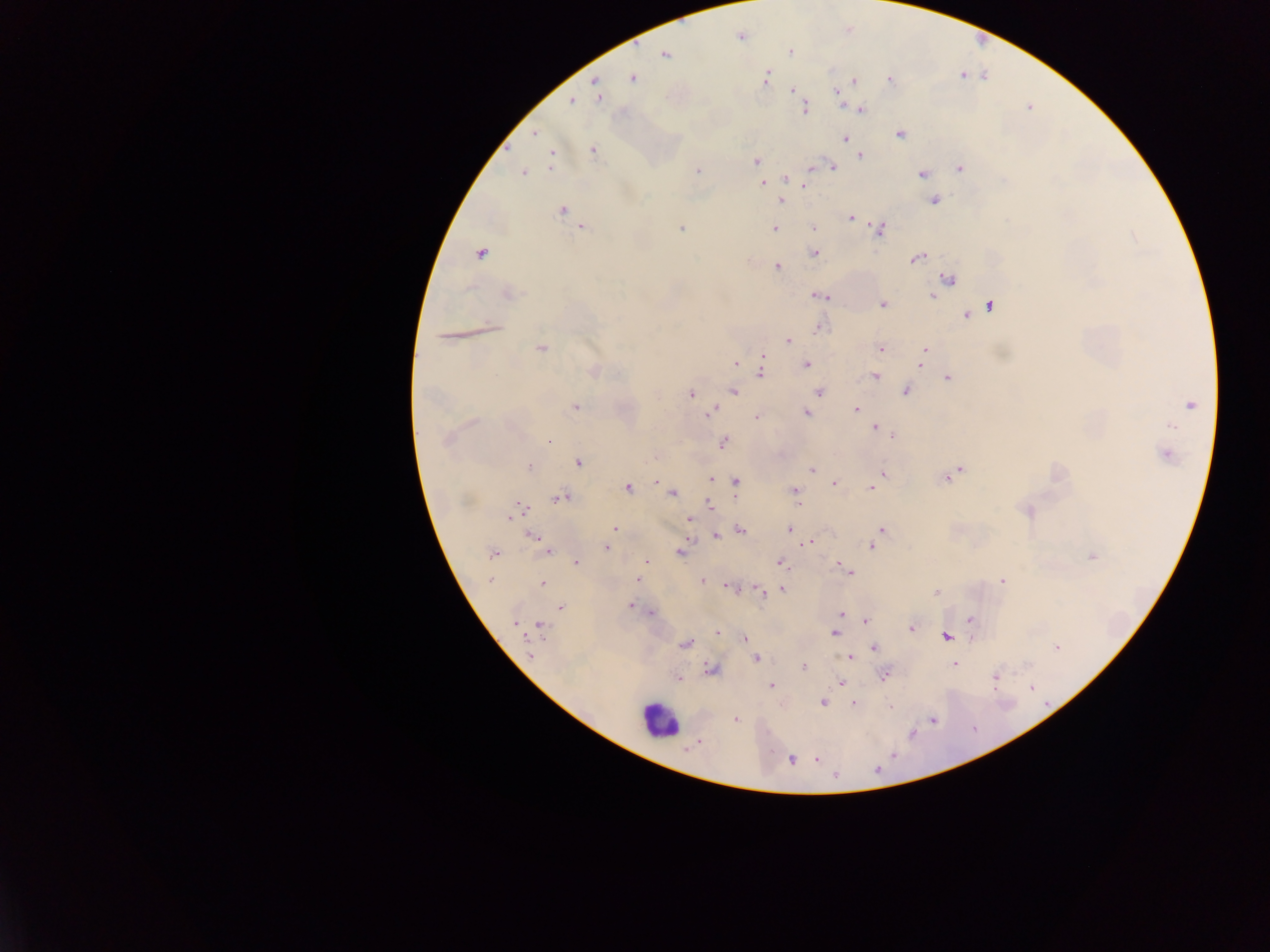

leukocyte locations = approximate centers as {x, y} in pixels: {657, 720}
field of view = single
country = Ghana
capture = mobile-phone photograph through a microscope
Plasmodium parasite locations = approximate centers as {x, y} in pixels: {740, 37}, {789, 51}, {665, 55}, {766, 78}, {632, 79}, {890, 80}, {854, 82}, {792, 90}, {837, 92}, {598, 95}, {571, 102}, {804, 108}, {860, 110}, {535, 133}, {901, 134}, {845, 138}, {593, 150}, {861, 156}, {551, 158}, {756, 160}, {831, 167}, {960, 168}, {698, 171}, {524, 172}, {922, 174}, {786, 179}, {762, 183}, {806, 185}, {781, 200}, {934, 201}, {562, 211}, {850, 217}, {583, 227}, {681, 228}, {814, 228}, {774, 229}, {879, 229}, {815, 253}, {480, 254}, {917, 257}, {777, 267}, {949, 278}, {509, 294}, {820, 295}, {933, 295}, {883, 304}, {989, 306}, {979, 311}, {966, 315}, {820, 327}, {490, 328}, {787, 340}, {541, 348}, {881, 349}, {925, 350}, {922, 356}, {763, 358}, {736, 363}, {920, 363}, {807, 365}, {593, 371}, {760, 371}, {875, 375}, {948, 378}, {734, 390}, {819, 391}, {906, 391}, {691, 394}, {1190, 404}, {576, 407}, {856, 410}, {711, 412}, {807, 413}, {757, 417}, {1171, 426}, {876, 428}, {890, 435}, {446, 440}, {550, 441}, {723, 442}, {1167, 455}, {579, 463}, {529, 467}, {812, 469}, {958, 472}, {884, 474}, {948, 478}, {710, 479}, {657, 481}, {736, 482}, {833, 483}, {628, 488}, {871, 489}, {795, 490}, {672, 493}, {559, 498}, {798, 503}, {711, 506}, {518, 509}, {1027, 511}, {512, 516}, {689, 520}, {615, 529}, {789, 529}, {741, 530}, {882, 530}, {716, 536}, {533, 537}, {810, 542}, {871, 546}, {606, 547}, {547, 551}, {680, 552}, {493, 554}, {1091, 557}, {647, 562}, {576, 563}, {780, 563}, {847, 571}, {637, 579}, {490, 580}, {1002, 580}, {702, 581}, {542, 583}, {729, 587}, {781, 590}, {760, 591}, {937, 592}, {630, 605}, {561, 607}, {634, 607}, {650, 613}, {842, 613}, {970, 619}, {866, 620}, {514, 623}, {539, 626}, {912, 628}, {717, 632}, {834, 633}, {745, 637}, {947, 637}, {685, 643}, {1056, 647}, {874, 648}, {529, 653}, {849, 657}, {756, 659}, {954, 665}, {804, 666}, {711, 670}, {884, 675}, {995, 676}, {678, 679}, {840, 683}, {772, 685}, {1031, 688}, {823, 702}, {855, 704}, {890, 706}, {736, 719}, {933, 720}, {792, 759}, {817, 760}, {877, 769}, {836, 776}
image size = 1270×952 pixels
preparation = thick blood smear